Give a bounding box for every malaria parasite.
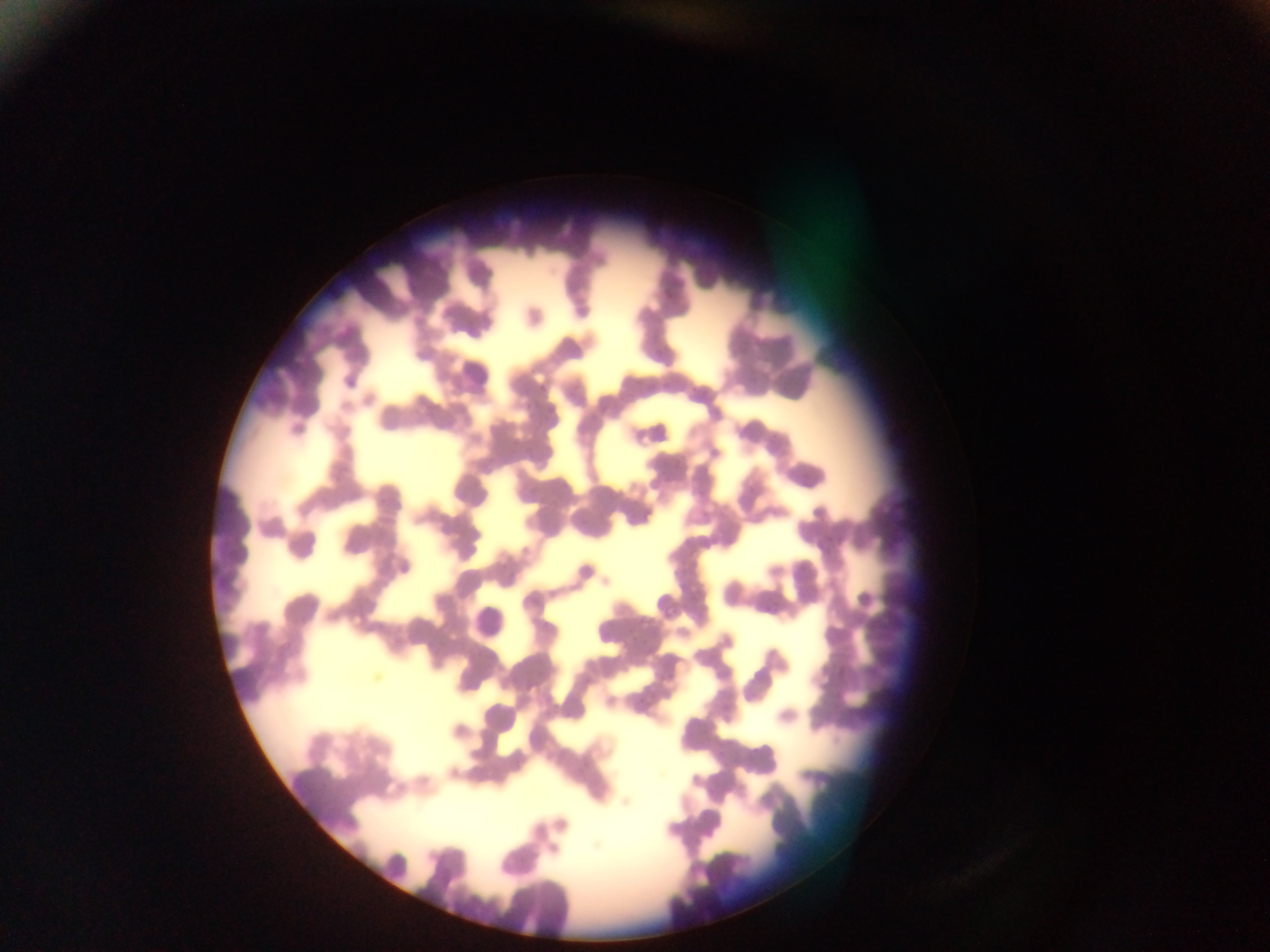

No malaria parasites observed.

{
  "leukocyte_locations": "approximate bounding boxes as {left, top, right, bottom} in pixels: {440, 345, 492, 402}, {283, 526, 323, 564}, {465, 597, 515, 651}, {474, 691, 522, 741}",
  "country": "Ghana",
  "image_size": "1270×952 pixels",
  "capture": "mobile-phone photograph through a microscope",
  "preparation": "thin blood smear",
  "field_of_view": "single"
}